Locate and identify every blood parasite.
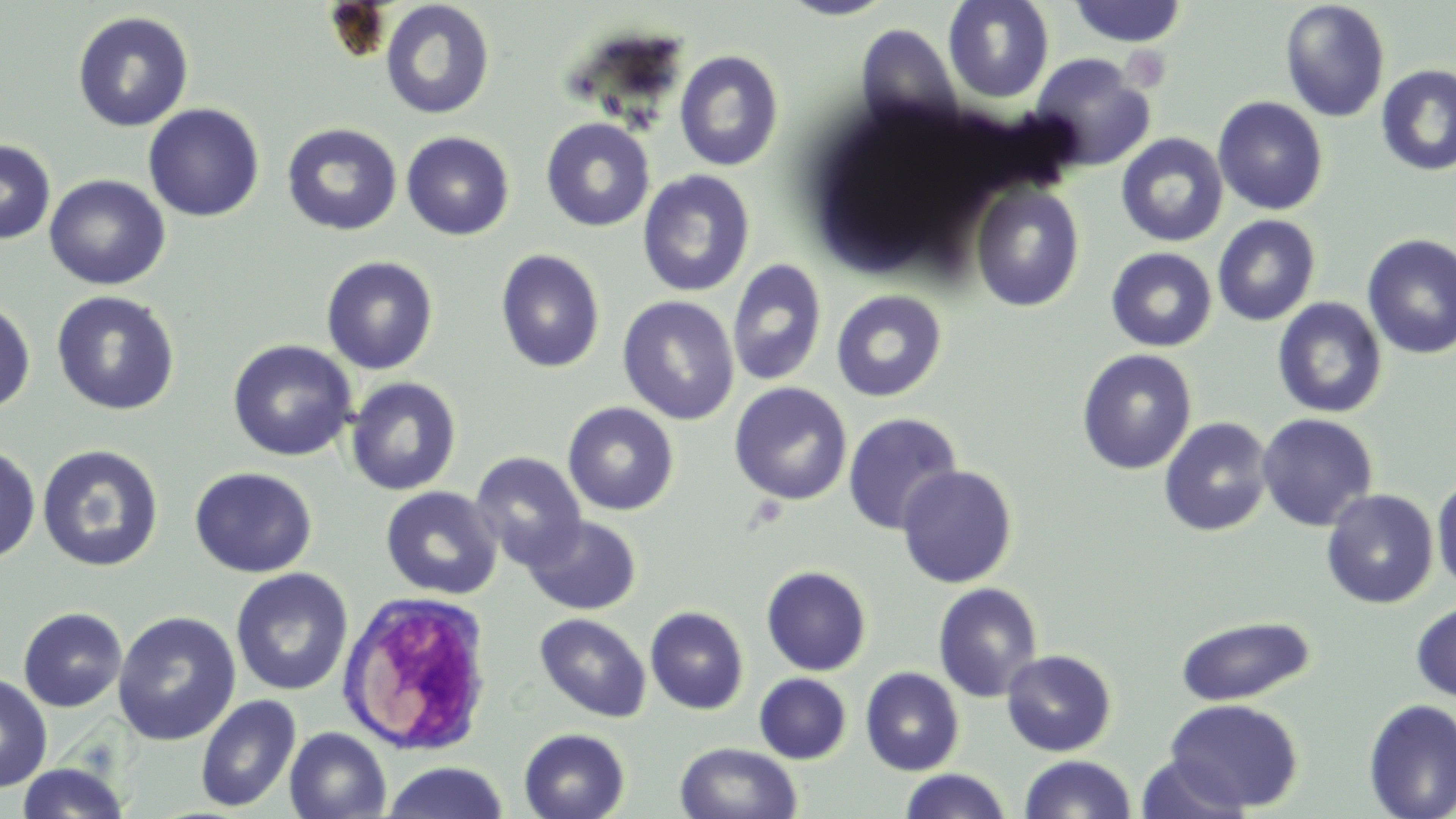
No blood parasites observed.

Approximate bounding boxes as [x1, y1, x2, y2] in pixels. Uninfected red blood cell locations: [778, 0, 898, 20], [943, 0, 1054, 104], [1279, 0, 1391, 123], [380, 1, 496, 120], [1067, 1, 1188, 47], [72, 11, 194, 133], [855, 23, 962, 132], [674, 50, 784, 171], [1029, 53, 1156, 172], [1376, 65, 1456, 176], [1212, 96, 1328, 215], [142, 103, 265, 223], [540, 118, 655, 232], [281, 123, 403, 236], [401, 131, 516, 241], [1116, 133, 1229, 248], [0, 138, 56, 245], [637, 169, 755, 298], [44, 174, 170, 290], [970, 182, 1085, 312], [1212, 214, 1321, 326], [1361, 233, 1456, 360], [1106, 247, 1217, 352], [495, 249, 606, 373], [321, 255, 439, 374], [726, 259, 827, 387], [830, 289, 948, 402], [51, 290, 180, 416], [617, 295, 740, 425], [0, 296, 36, 416], [1273, 297, 1388, 418], [227, 339, 358, 462], [1076, 348, 1197, 475], [345, 376, 462, 496], [729, 383, 852, 505], [562, 402, 680, 516], [842, 412, 964, 536], [1256, 413, 1378, 532], [1158, 416, 1274, 536], [36, 443, 164, 572], [0, 444, 41, 565], [471, 451, 586, 570], [896, 464, 1018, 589], [189, 466, 317, 578], [1432, 472, 1456, 594], [380, 486, 503, 600], [1321, 488, 1439, 608], [523, 515, 641, 615], [761, 566, 872, 676], [230, 568, 353, 697], [932, 582, 1044, 702], [1411, 598, 1456, 703], [645, 606, 749, 715], [17, 607, 128, 712], [112, 611, 241, 746], [535, 613, 651, 723], [1175, 615, 1315, 707], [1001, 649, 1117, 757], [860, 667, 965, 776], [0, 672, 53, 792], [754, 673, 851, 764], [195, 693, 302, 813], [1164, 698, 1303, 813], [1363, 699, 1456, 818], [284, 727, 391, 818], [519, 728, 630, 819], [675, 741, 803, 819], [1019, 754, 1136, 819], [1135, 755, 1252, 818], [380, 761, 509, 819], [16, 762, 131, 818], [898, 769, 1012, 819]. White blood cell locations: [336, 591, 496, 756]. Slide-level diagnosis: negative for blood parasites. Single field of view. Optical microscopy. Thin blood film. May-Grünwald-Giemsa-stained preparation. Captured at 1000x magnification. Image is 1456×819 pixels.